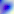
Toxoplasma gondii is seen. 400x magnification. Micrograph.